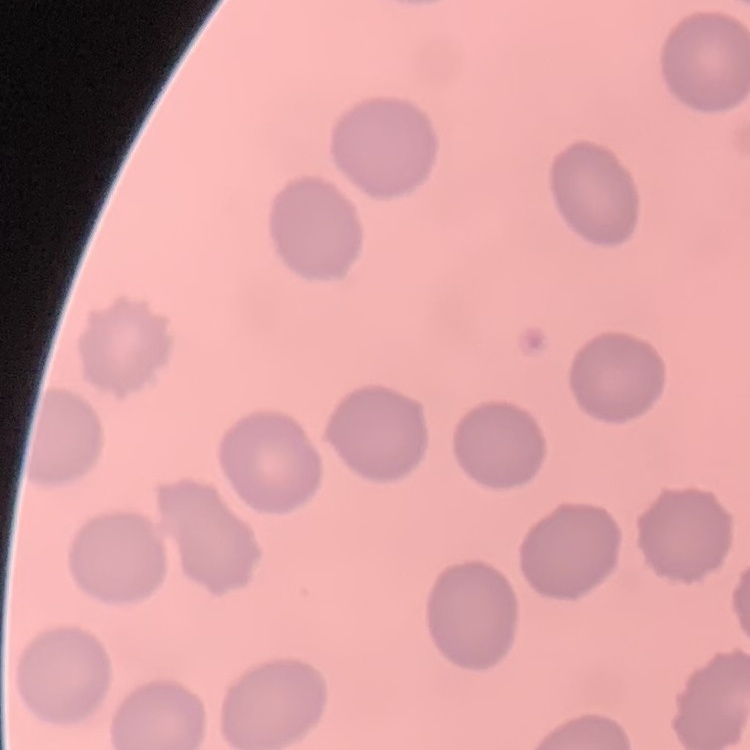 The erythrocytes exhibit no rouleaux formation. Thin peripheral smear. Field's or Giemsa stain. Square crop of a larger photomicrograph.